Assess the morphology of the red blood cells.
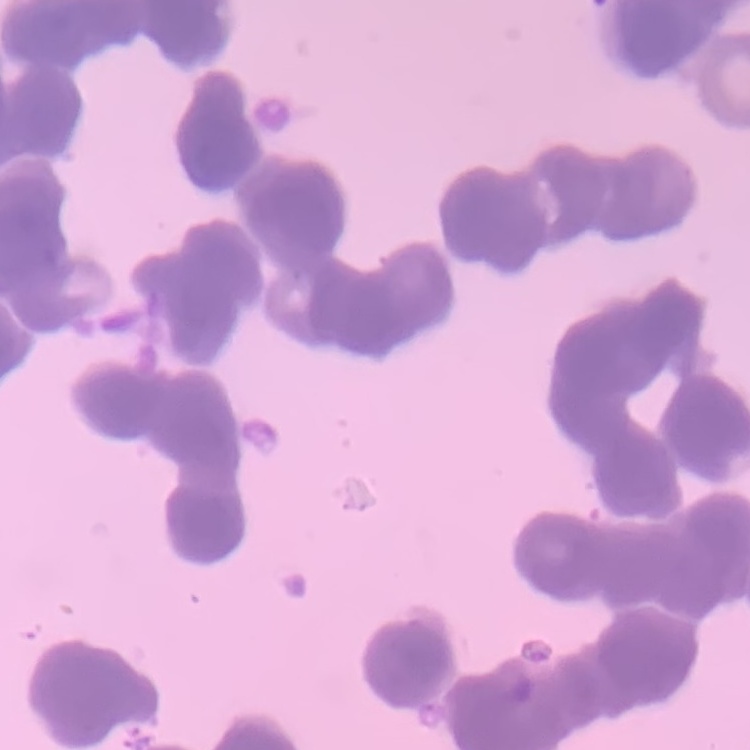

Rouleaux formation.

Summary:
  - Preparation: thin blood smear
  - Image type: one tile cut from a larger photomicrograph
  - Stain: Field's or Giemsa